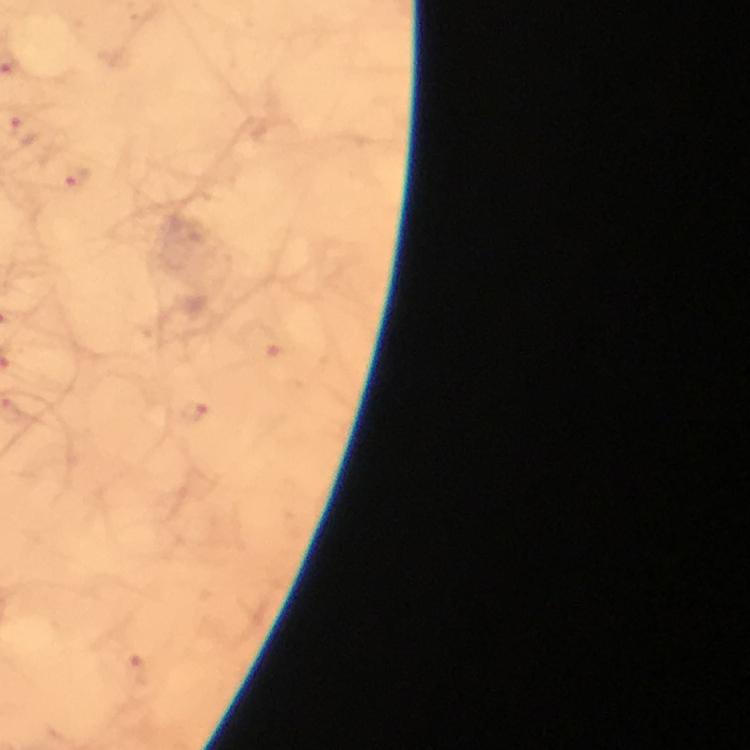
Approximate centers as {x, y} in pixels.
Summary:
  - Malaria parasite locations: {76, 179}, {194, 413}, {141, 673}
  - Immersion oil: used
  - Context: from a malaria diagnostic workup
  - Stain: Giemsa
  - Cropped from: one field of view
  - Magnification: 100x
  - Capture: smartphone camera through the microscope
  - Image size: 750×750 pixels
  - Preparation: thick smear